State which cell type is depicted.
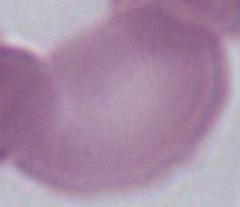
An erythrocyte.

Summary:
  - Magnification: 1000x
  - Modality: photomicrograph